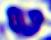 Captured at 400x magnification. A white blood cell is seen. Micrograph.